Locate every blood parasite and identify its species.
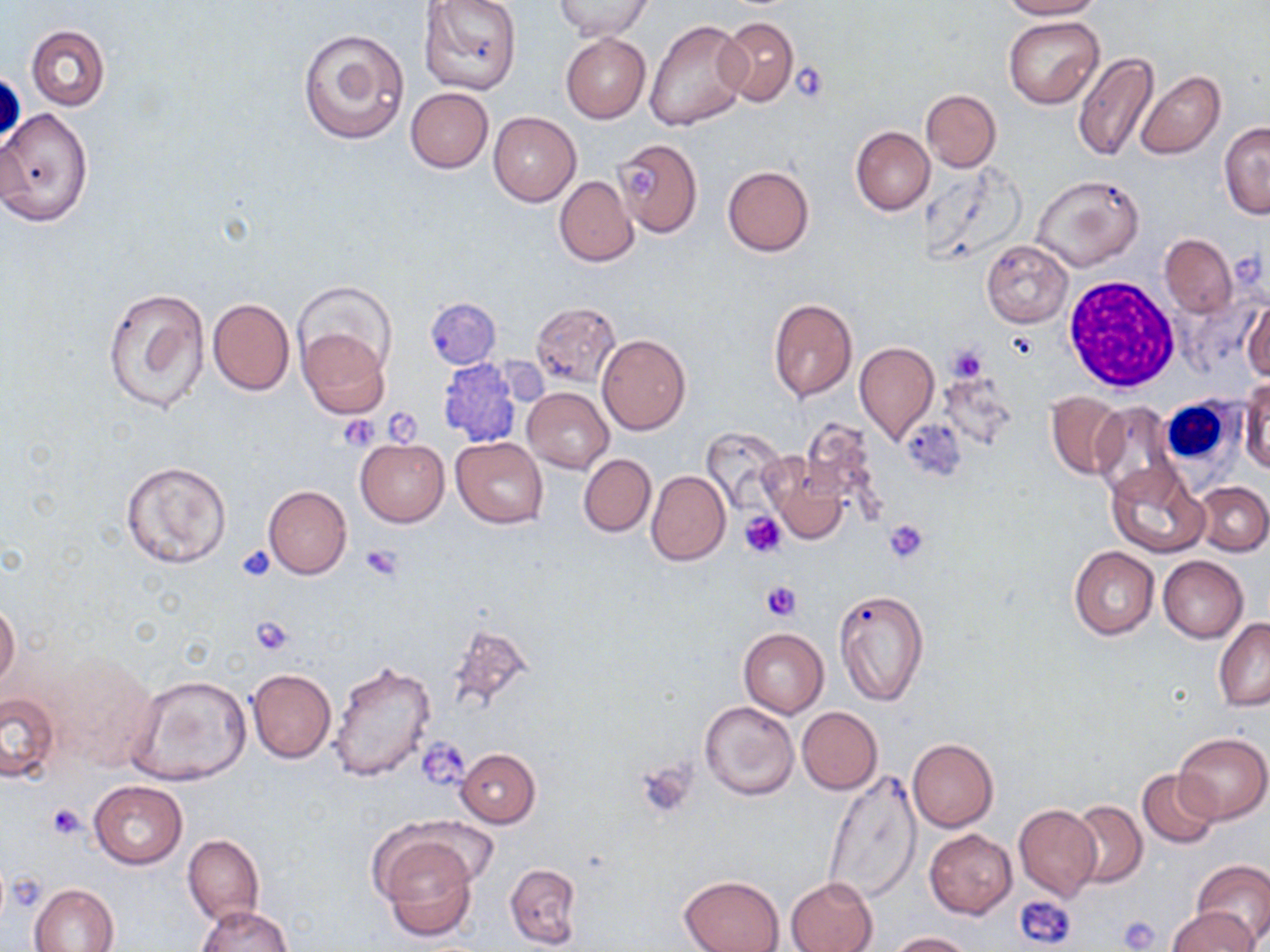
No blood parasites seen.

Approximate bounding boxes as named x1/y1/x2/y2 corners in pixels. Uninfected red blood cell locations: (x1=418, y1=0, x2=523, y2=97), (x1=555, y1=0, x2=651, y2=39), (x1=1001, y1=0, x2=1102, y2=19), (x1=1004, y1=16, x2=1104, y2=108), (x1=644, y1=17, x2=749, y2=131), (x1=718, y1=17, x2=798, y2=106), (x1=27, y1=25, x2=109, y2=111), (x1=299, y1=28, x2=411, y2=145), (x1=561, y1=34, x2=650, y2=121), (x1=1073, y1=51, x2=1158, y2=163), (x1=1135, y1=70, x2=1226, y2=160), (x1=405, y1=87, x2=492, y2=173), (x1=922, y1=89, x2=1000, y2=171), (x1=0, y1=106, x2=93, y2=228), (x1=489, y1=112, x2=582, y2=206), (x1=1219, y1=121, x2=1269, y2=218), (x1=851, y1=126, x2=934, y2=215), (x1=612, y1=138, x2=703, y2=237), (x1=722, y1=165, x2=814, y2=256), (x1=1030, y1=172, x2=1145, y2=272), (x1=554, y1=176, x2=638, y2=266), (x1=1159, y1=234, x2=1237, y2=318), (x1=981, y1=241, x2=1072, y2=326), (x1=293, y1=282, x2=398, y2=378), (x1=102, y1=287, x2=211, y2=414), (x1=207, y1=298, x2=294, y2=395), (x1=769, y1=298, x2=857, y2=401), (x1=1243, y1=301, x2=1270, y2=383), (x1=531, y1=302, x2=621, y2=388), (x1=298, y1=326, x2=391, y2=420), (x1=596, y1=334, x2=691, y2=435), (x1=852, y1=340, x2=939, y2=446), (x1=1241, y1=377, x2=1269, y2=474), (x1=523, y1=387, x2=613, y2=473), (x1=1046, y1=393, x2=1124, y2=478), (x1=1089, y1=401, x2=1181, y2=501), (x1=699, y1=426, x2=787, y2=514), (x1=452, y1=436, x2=549, y2=528), (x1=356, y1=439, x2=449, y2=527), (x1=766, y1=453, x2=850, y2=543), (x1=578, y1=454, x2=655, y2=536), (x1=121, y1=459, x2=233, y2=570), (x1=1106, y1=461, x2=1207, y2=557), (x1=647, y1=470, x2=730, y2=566), (x1=1195, y1=482, x2=1270, y2=555), (x1=263, y1=485, x2=352, y2=579), (x1=1068, y1=546, x2=1159, y2=640), (x1=1158, y1=556, x2=1248, y2=642), (x1=833, y1=588, x2=930, y2=706), (x1=0, y1=602, x2=20, y2=691), (x1=1214, y1=617, x2=1270, y2=711), (x1=443, y1=626, x2=535, y2=720), (x1=737, y1=627, x2=829, y2=718), (x1=46, y1=649, x2=161, y2=771), (x1=328, y1=660, x2=434, y2=783), (x1=247, y1=668, x2=335, y2=763), (x1=126, y1=675, x2=252, y2=786), (x1=0, y1=692, x2=60, y2=782), (x1=700, y1=701, x2=800, y2=801), (x1=797, y1=706, x2=882, y2=794), (x1=1174, y1=731, x2=1269, y2=823), (x1=907, y1=739, x2=999, y2=832), (x1=455, y1=748, x2=541, y2=828), (x1=822, y1=768, x2=921, y2=905), (x1=1137, y1=768, x2=1219, y2=849), (x1=89, y1=781, x2=187, y2=868), (x1=1069, y1=801, x2=1146, y2=888), (x1=1014, y1=805, x2=1101, y2=901), (x1=925, y1=829, x2=1016, y2=918), (x1=374, y1=830, x2=482, y2=940), (x1=183, y1=833, x2=264, y2=926), (x1=1192, y1=860, x2=1270, y2=946), (x1=504, y1=863, x2=581, y2=949), (x1=679, y1=876, x2=783, y2=952), (x1=787, y1=876, x2=877, y2=952), (x1=30, y1=883, x2=119, y2=951), (x1=195, y1=904, x2=292, y2=952), (x1=1168, y1=906, x2=1260, y2=951), (x1=885, y1=931, x2=973, y2=951). Platelet locations: (x1=793, y1=61, x2=829, y2=102), (x1=628, y1=161, x2=655, y2=204), (x1=946, y1=344, x2=990, y2=382), (x1=381, y1=410, x2=421, y2=444), (x1=338, y1=414, x2=381, y2=451), (x1=740, y1=512, x2=785, y2=559), (x1=884, y1=518, x2=930, y2=563), (x1=236, y1=545, x2=276, y2=580), (x1=361, y1=545, x2=401, y2=579), (x1=762, y1=580, x2=799, y2=620), (x1=250, y1=617, x2=294, y2=655), (x1=419, y1=738, x2=472, y2=793), (x1=635, y1=756, x2=692, y2=814), (x1=47, y1=803, x2=85, y2=840), (x1=1017, y1=897, x2=1077, y2=948), (x1=1119, y1=915, x2=1159, y2=950). White blood cell locations: (x1=1063, y1=275, x2=1180, y2=392), (x1=1159, y1=399, x2=1237, y2=473). Slide-level diagnosis: negative for blood parasites. Single field of view. Optical microscopy. Image is 1270×952 pixels. May-Grünwald-Giemsa-stained preparation. Thin blood smear. 1000x magnification.